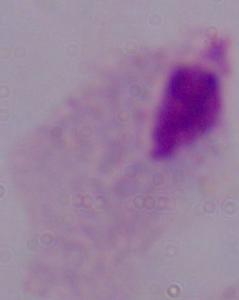
Micrograph. A trichomonad is seen. Captured at 1000x magnification.